Outline each blood parasite and name the species.
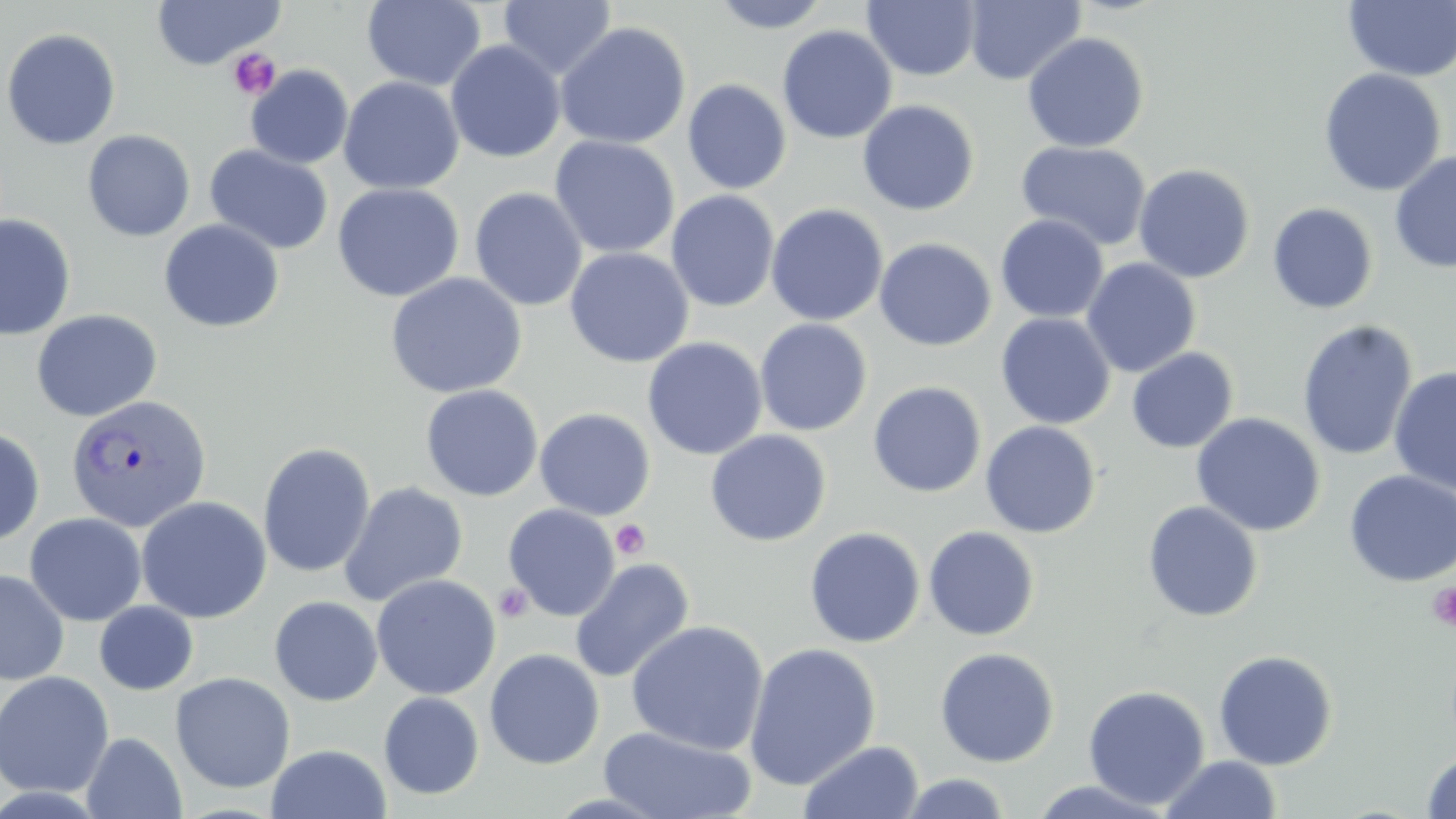

Approximate bounding boxes as named x1/y1/x2/y2 corners in pixels.
Plasmodium vivax-infected red blood cells: (x1=65, y1=393, x2=212, y2=532).
No Plasmodium falciparum, Plasmodium ovale, Plasmodium malariae, Babesia divergens, or Trypanosoma brucei observed.

slide-level diagnosis = Plasmodium vivax
uninfected red blood cell locations = approximate bounding boxes as named x1/y1/x2/y2 corners in pixels: (x1=362, y1=0, x2=487, y2=91), (x1=498, y1=0, x2=616, y2=81), (x1=708, y1=0, x2=833, y2=34), (x1=963, y1=0, x2=1087, y2=86), (x1=1343, y1=0, x2=1456, y2=82), (x1=151, y1=1, x2=285, y2=69), (x1=863, y1=1, x2=982, y2=81), (x1=554, y1=21, x2=691, y2=149), (x1=777, y1=25, x2=897, y2=144), (x1=0, y1=27, x2=122, y2=150), (x1=1022, y1=32, x2=1150, y2=152), (x1=445, y1=40, x2=566, y2=163), (x1=245, y1=65, x2=354, y2=169), (x1=1318, y1=68, x2=1446, y2=197), (x1=338, y1=76, x2=465, y2=195), (x1=682, y1=79, x2=792, y2=195), (x1=856, y1=99, x2=980, y2=216), (x1=82, y1=130, x2=196, y2=242), (x1=549, y1=135, x2=680, y2=259), (x1=1016, y1=140, x2=1153, y2=251), (x1=204, y1=144, x2=334, y2=255), (x1=1389, y1=151, x2=1456, y2=273), (x1=1020, y1=155, x2=1257, y2=268), (x1=1133, y1=164, x2=1255, y2=283), (x1=331, y1=182, x2=465, y2=303), (x1=469, y1=187, x2=588, y2=312), (x1=665, y1=190, x2=780, y2=312), (x1=766, y1=203, x2=888, y2=326), (x1=1267, y1=203, x2=1379, y2=315), (x1=1, y1=214, x2=76, y2=341), (x1=995, y1=214, x2=1109, y2=323), (x1=158, y1=219, x2=285, y2=333), (x1=874, y1=237, x2=997, y2=351), (x1=565, y1=247, x2=694, y2=368), (x1=1081, y1=258, x2=1201, y2=378), (x1=384, y1=272, x2=528, y2=399), (x1=30, y1=309, x2=162, y2=422), (x1=996, y1=312, x2=1116, y2=430), (x1=754, y1=318, x2=873, y2=436), (x1=1297, y1=319, x2=1418, y2=462), (x1=642, y1=336, x2=767, y2=460), (x1=1126, y1=347, x2=1238, y2=453), (x1=1388, y1=366, x2=1456, y2=496), (x1=867, y1=381, x2=987, y2=498), (x1=419, y1=384, x2=544, y2=502), (x1=534, y1=407, x2=656, y2=521), (x1=1190, y1=413, x2=1326, y2=537), (x1=980, y1=421, x2=1101, y2=538), (x1=0, y1=426, x2=45, y2=547), (x1=705, y1=429, x2=832, y2=546), (x1=257, y1=442, x2=376, y2=579), (x1=1343, y1=470, x2=1456, y2=588), (x1=338, y1=481, x2=468, y2=607), (x1=135, y1=496, x2=272, y2=623), (x1=1142, y1=500, x2=1263, y2=622), (x1=502, y1=503, x2=619, y2=621), (x1=24, y1=512, x2=148, y2=626), (x1=923, y1=525, x2=1040, y2=641), (x1=804, y1=527, x2=925, y2=648), (x1=569, y1=557, x2=695, y2=683), (x1=0, y1=569, x2=69, y2=685), (x1=371, y1=573, x2=501, y2=700), (x1=269, y1=596, x2=383, y2=706), (x1=94, y1=601, x2=198, y2=695), (x1=626, y1=620, x2=769, y2=755), (x1=743, y1=642, x2=882, y2=790), (x1=935, y1=647, x2=1060, y2=767), (x1=484, y1=648, x2=604, y2=770), (x1=1213, y1=650, x2=1339, y2=770), (x1=0, y1=671, x2=114, y2=798), (x1=170, y1=672, x2=295, y2=793), (x1=1083, y1=685, x2=1210, y2=810), (x1=378, y1=692, x2=485, y2=800), (x1=598, y1=725, x2=758, y2=819), (x1=80, y1=732, x2=187, y2=818), (x1=799, y1=741, x2=924, y2=819), (x1=266, y1=744, x2=392, y2=818), (x1=1420, y1=750, x2=1456, y2=818), (x1=1159, y1=755, x2=1281, y2=818), (x1=898, y1=772, x2=1012, y2=818), (x1=1024, y1=778, x2=1175, y2=818)
modality = light microscopy
platelet locations = approximate bounding boxes as named x1/y1/x2/y2 corners in pixels: (x1=228, y1=48, x2=282, y2=99), (x1=611, y1=518, x2=652, y2=561), (x1=1427, y1=582, x2=1456, y2=631), (x1=493, y1=583, x2=533, y2=623)
preparation = thin blood film
field of view = one of a larger specimen
magnification = 1000x
image size = 1456×819 pixels
stain = May-Grünwald-Giemsa